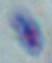
magnification = 1000x
modality = photomicrograph
identification = Toxoplasma gondii